Report the malaria status of this cell.
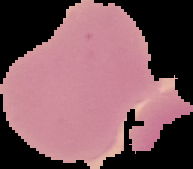
It is uninfected.

image size = 193×169 pixels
preparation = thin blood film
image type = segmented cell region with the area outside set to black